Comment on the morphology of the red blood cells.
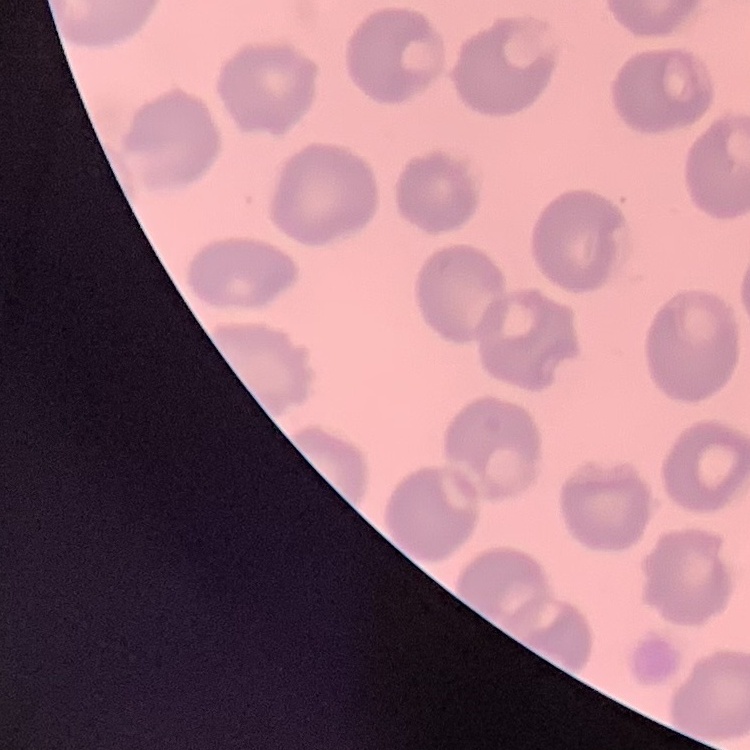

They show no rouleaux formation.

One tile cut from a larger photomicrograph. Stained with either Field's or Giemsa. Thin blood film.